Classify this cell by malaria status.
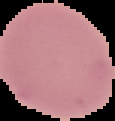

It is uninfected.

Image is 115×121 pixels. Segmented cell region on a black background. From a thin blood film.